Identify the blood parasite species.
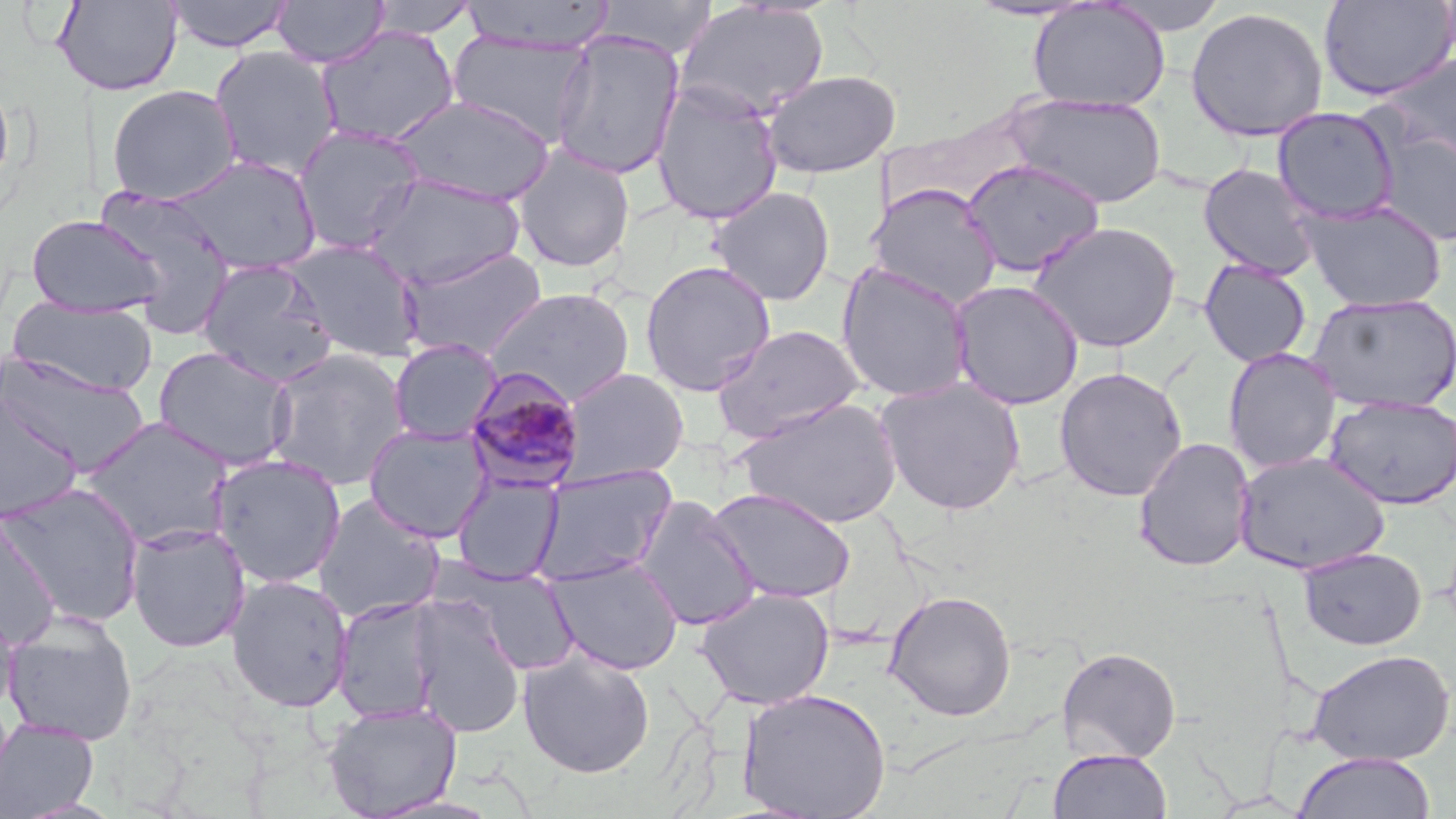
Plasmodium malariae.

Approximate bounding boxes as [x1, y1, x2, y2] in pixels. Uninfected red blood cell locations: [163, 0, 295, 53], [271, 0, 389, 69], [591, 0, 718, 58], [1099, 0, 1231, 35], [1318, 0, 1456, 101], [52, 1, 183, 96], [366, 1, 483, 39], [458, 1, 616, 52], [1028, 1, 1171, 111], [673, 2, 831, 122], [1185, 6, 1329, 143], [315, 25, 460, 148], [549, 31, 686, 180], [447, 33, 595, 146], [208, 46, 343, 181], [1375, 50, 1456, 171], [761, 70, 901, 179], [0, 79, 15, 200], [650, 81, 784, 224], [106, 84, 241, 205], [1003, 93, 1168, 208], [388, 95, 557, 205], [1271, 107, 1400, 224], [291, 124, 427, 256], [1372, 125, 1456, 248], [512, 146, 636, 273], [166, 154, 323, 276], [961, 159, 1106, 277], [1198, 163, 1322, 280], [365, 172, 526, 292], [867, 183, 1002, 308], [93, 186, 238, 335], [709, 187, 835, 306], [1298, 199, 1448, 312], [26, 215, 167, 318], [1027, 220, 1183, 353], [284, 239, 425, 362], [398, 246, 548, 362], [196, 258, 338, 385], [1198, 259, 1312, 367], [639, 260, 776, 396], [835, 261, 975, 402], [948, 279, 1085, 410], [485, 287, 636, 406], [1305, 293, 1456, 414], [6, 297, 158, 395], [710, 324, 866, 444], [388, 338, 503, 445], [152, 345, 297, 471], [1223, 347, 1342, 473], [262, 348, 412, 492], [0, 352, 151, 478], [559, 367, 690, 485], [1054, 367, 1188, 501], [875, 377, 1026, 515], [1, 390, 84, 525], [1323, 395, 1456, 510], [734, 396, 903, 529], [78, 416, 236, 550], [363, 423, 493, 542], [1133, 437, 1256, 572], [1233, 451, 1391, 575], [209, 453, 347, 589], [530, 465, 677, 586], [452, 475, 564, 583], [1, 481, 146, 628], [707, 486, 856, 603], [313, 494, 446, 624], [633, 495, 760, 630], [0, 517, 61, 650], [126, 523, 251, 653], [1298, 546, 1427, 650], [545, 556, 684, 675], [442, 562, 583, 675], [226, 575, 354, 713], [695, 587, 835, 709], [883, 589, 1017, 721], [332, 596, 443, 723], [407, 596, 525, 738], [0, 602, 19, 720], [2, 611, 138, 746], [1056, 646, 1182, 764], [518, 648, 656, 778], [1307, 648, 1454, 765], [737, 687, 892, 819], [322, 701, 463, 818], [0, 718, 100, 819], [1048, 748, 1172, 819], [1293, 752, 1436, 819], [367, 793, 507, 819]. Plasmodium malariae-infected red blood cell locations: [464, 367, 587, 493]. Thin blood smear. May-Grünwald-Giemsa-stained preparation. Image is 1456×819 pixels. Single field of view. 1000x magnification. Optical microscopy.